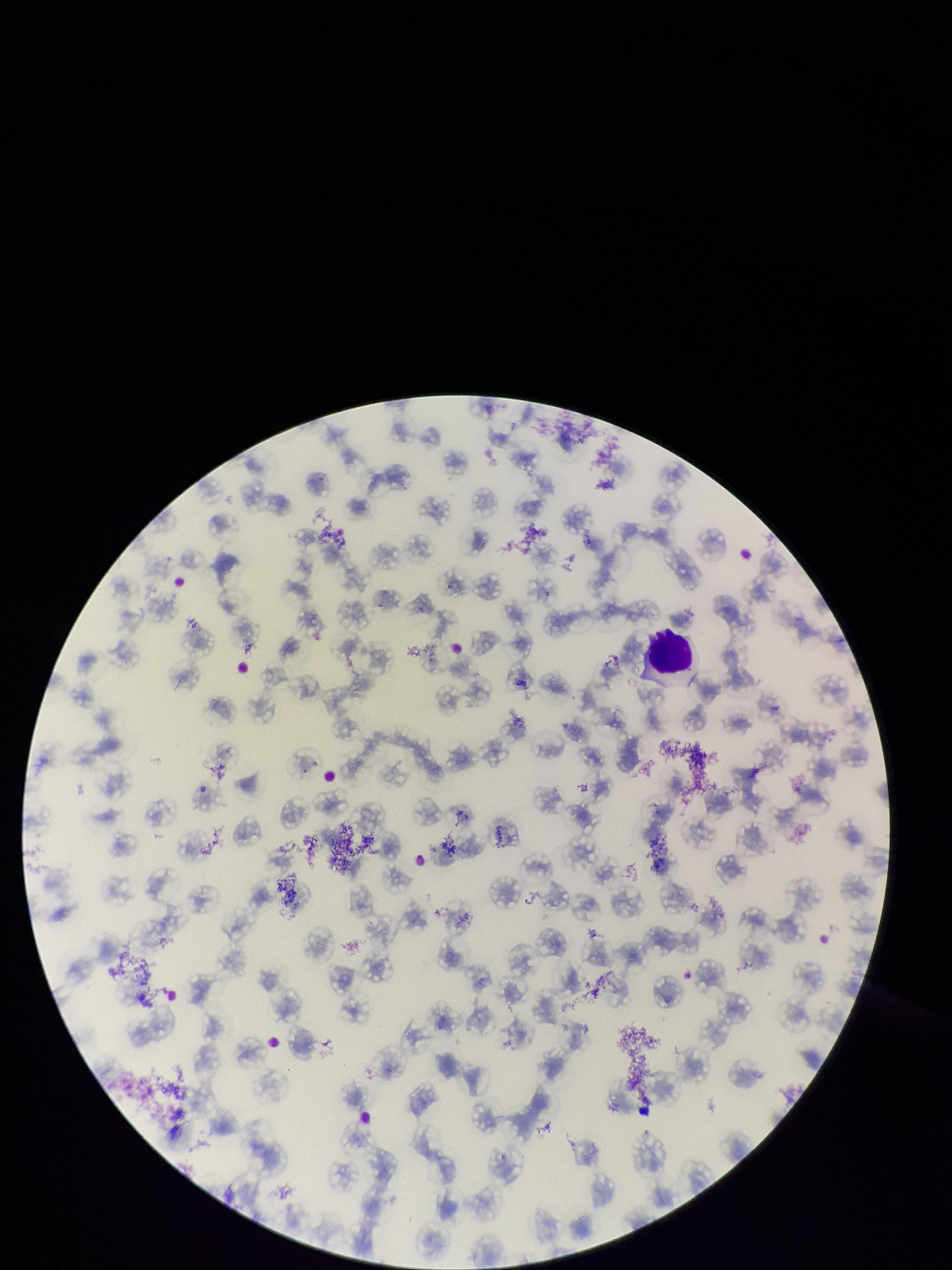

species reported for this patient = Plasmodium falciparum
patient malaria status = positive
parasitized red blood cells = none seen
preparation = thin smear
image size = 952×1270 pixels
stain = Giemsa
field of view = one from this slide
red blood cell count = 96
capture = smartphone photograph through the microscope eyepiece
parasitized red blood cell count = 0